Locate and identify every blood parasite.
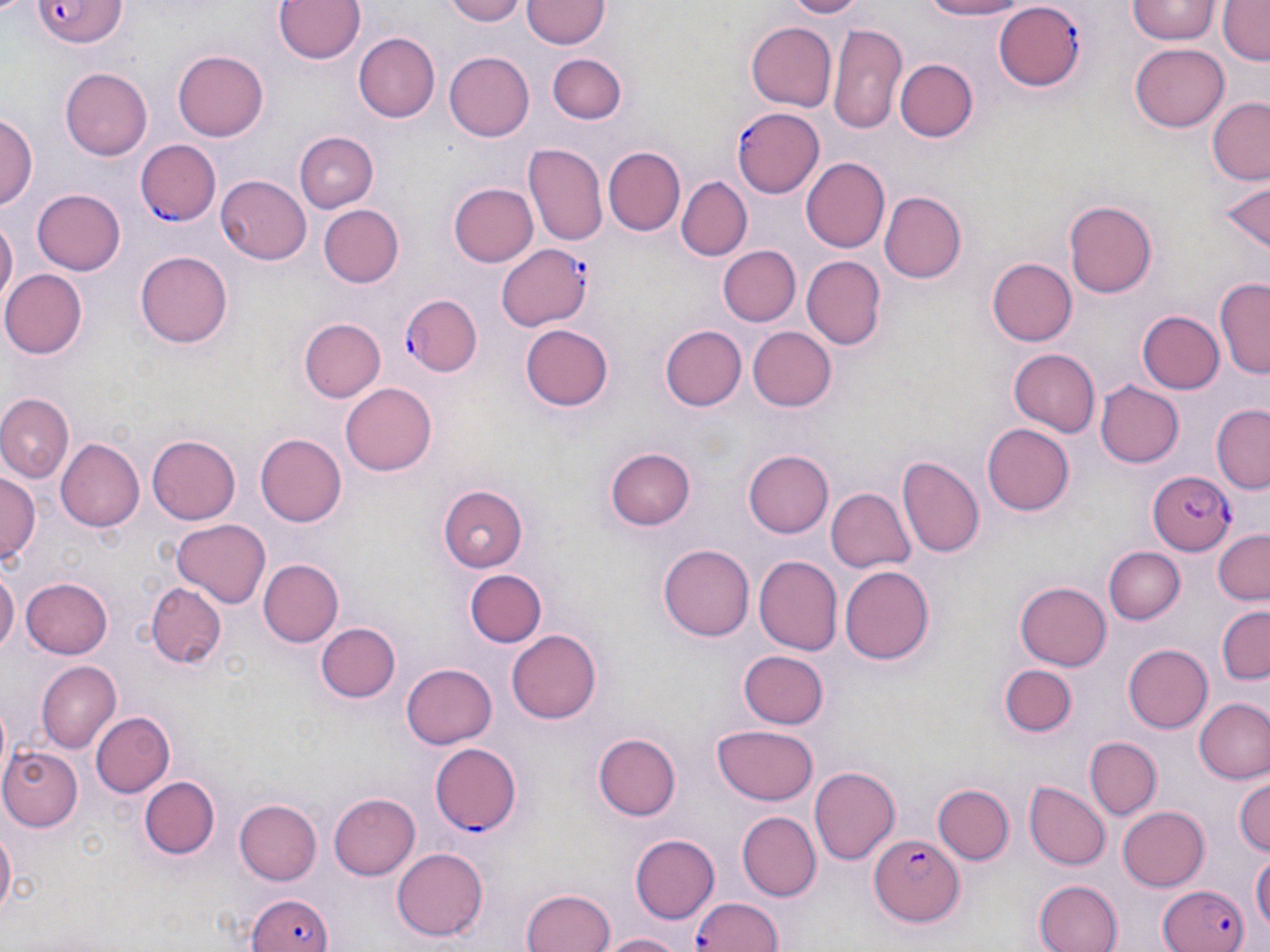

Approximate bounding boxes as named x1/y1/x2/y2 corners in pixels.
Plasmodium falciparum-infected red blood cells: (x1=30, y1=0, x2=130, y2=50), (x1=994, y1=1, x2=1086, y2=89), (x1=733, y1=107, x2=827, y2=199), (x1=139, y1=140, x2=220, y2=225), (x1=494, y1=244, x2=594, y2=332), (x1=402, y1=295, x2=481, y2=377), (x1=1148, y1=469, x2=1236, y2=554), (x1=429, y1=743, x2=520, y2=835), (x1=870, y1=832, x2=965, y2=926), (x1=1157, y1=881, x2=1248, y2=952), (x1=248, y1=891, x2=336, y2=952), (x1=690, y1=896, x2=786, y2=952).
No Plasmodium ovale, Plasmodium malariae, Plasmodium vivax, Babesia divergens, or Trypanosoma brucei observed.

slide-level diagnosis = Plasmodium falciparum
stain = May-Grünwald-Giemsa
image size = 1270×952 pixels
modality = optical microscopy
magnification = 1000x
field of view = one of a larger specimen
uninfected red blood cell locations = approximate bounding boxes as named x1/y1/x2/y2 corners in pixels: (x1=272, y1=0, x2=368, y2=66), (x1=442, y1=0, x2=530, y2=25), (x1=781, y1=0, x2=863, y2=18), (x1=918, y1=0, x2=1033, y2=20), (x1=1125, y1=0, x2=1221, y2=45), (x1=1218, y1=0, x2=1269, y2=64), (x1=521, y1=1, x2=608, y2=48), (x1=538, y1=9, x2=616, y2=115), (x1=746, y1=22, x2=838, y2=112), (x1=829, y1=22, x2=906, y2=133), (x1=353, y1=34, x2=439, y2=121), (x1=1131, y1=42, x2=1229, y2=132), (x1=173, y1=48, x2=269, y2=143), (x1=551, y1=52, x2=627, y2=123), (x1=445, y1=53, x2=534, y2=141), (x1=895, y1=60, x2=978, y2=142), (x1=61, y1=67, x2=152, y2=160), (x1=1205, y1=97, x2=1270, y2=183), (x1=1, y1=114, x2=38, y2=210), (x1=302, y1=125, x2=389, y2=276), (x1=295, y1=133, x2=379, y2=212), (x1=522, y1=144, x2=607, y2=248), (x1=602, y1=147, x2=685, y2=235), (x1=802, y1=158, x2=891, y2=253), (x1=216, y1=175, x2=312, y2=265), (x1=678, y1=177, x2=751, y2=260), (x1=1215, y1=180, x2=1269, y2=254), (x1=448, y1=184, x2=538, y2=266), (x1=32, y1=188, x2=127, y2=274), (x1=880, y1=190, x2=969, y2=285), (x1=1063, y1=200, x2=1156, y2=298), (x1=317, y1=203, x2=404, y2=289), (x1=0, y1=219, x2=17, y2=309), (x1=717, y1=245, x2=799, y2=327), (x1=136, y1=248, x2=232, y2=346), (x1=802, y1=256, x2=885, y2=350), (x1=987, y1=258, x2=1076, y2=345), (x1=2, y1=269, x2=88, y2=358), (x1=1217, y1=276, x2=1270, y2=380), (x1=1137, y1=310, x2=1223, y2=393), (x1=298, y1=318, x2=386, y2=403), (x1=521, y1=324, x2=613, y2=412), (x1=660, y1=325, x2=746, y2=411), (x1=748, y1=327, x2=836, y2=411), (x1=1007, y1=349, x2=1101, y2=437), (x1=341, y1=380, x2=437, y2=473), (x1=1095, y1=380, x2=1184, y2=468), (x1=0, y1=396, x2=73, y2=482), (x1=1210, y1=406, x2=1269, y2=493), (x1=982, y1=424, x2=1075, y2=516), (x1=255, y1=431, x2=348, y2=527), (x1=148, y1=435, x2=242, y2=523), (x1=56, y1=438, x2=145, y2=532), (x1=606, y1=448, x2=695, y2=531), (x1=742, y1=449, x2=832, y2=538), (x1=900, y1=457, x2=985, y2=559), (x1=1, y1=473, x2=39, y2=565), (x1=437, y1=485, x2=531, y2=570), (x1=824, y1=485, x2=916, y2=575), (x1=172, y1=518, x2=274, y2=607), (x1=1209, y1=528, x2=1270, y2=606), (x1=659, y1=544, x2=753, y2=642), (x1=1105, y1=545, x2=1184, y2=624), (x1=755, y1=556, x2=841, y2=654), (x1=258, y1=559, x2=345, y2=647), (x1=840, y1=566, x2=935, y2=664), (x1=0, y1=567, x2=17, y2=661), (x1=464, y1=570, x2=545, y2=648), (x1=22, y1=577, x2=113, y2=659), (x1=146, y1=578, x2=228, y2=670), (x1=1017, y1=579, x2=1113, y2=670), (x1=1216, y1=605, x2=1269, y2=684), (x1=315, y1=620, x2=401, y2=702), (x1=507, y1=628, x2=602, y2=723), (x1=1123, y1=643, x2=1213, y2=733), (x1=740, y1=650, x2=828, y2=727), (x1=35, y1=660, x2=120, y2=752), (x1=401, y1=662, x2=497, y2=750), (x1=1001, y1=666, x2=1076, y2=736), (x1=1194, y1=697, x2=1270, y2=785), (x1=0, y1=702, x2=13, y2=783), (x1=90, y1=711, x2=175, y2=797), (x1=712, y1=724, x2=820, y2=805), (x1=593, y1=732, x2=681, y2=820), (x1=1084, y1=737, x2=1161, y2=820), (x1=2, y1=746, x2=81, y2=830), (x1=809, y1=765, x2=900, y2=867), (x1=139, y1=775, x2=220, y2=859), (x1=1234, y1=775, x2=1269, y2=860), (x1=1027, y1=782, x2=1110, y2=870), (x1=933, y1=784, x2=1014, y2=867), (x1=327, y1=792, x2=420, y2=881), (x1=233, y1=798, x2=321, y2=886), (x1=1118, y1=805, x2=1210, y2=891), (x1=737, y1=811, x2=821, y2=900), (x1=0, y1=817, x2=16, y2=923), (x1=629, y1=834, x2=719, y2=924), (x1=392, y1=848, x2=489, y2=940), (x1=1251, y1=849, x2=1269, y2=938), (x1=1033, y1=878, x2=1122, y2=952), (x1=520, y1=886, x2=616, y2=952), (x1=602, y1=930, x2=686, y2=952)
preparation = thin blood film